Point out each leukocyte.
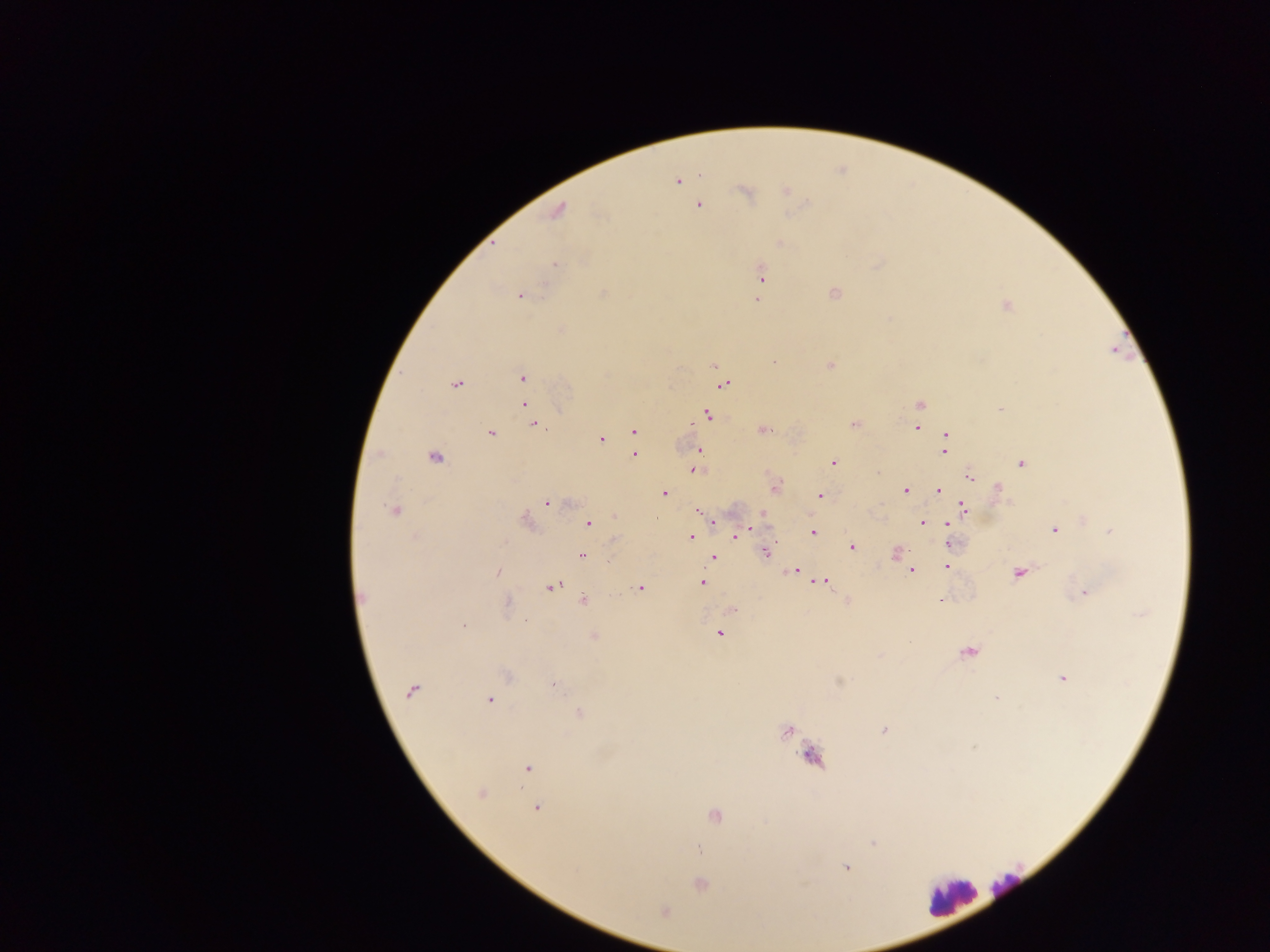
Approximate centers as [x, y] in pixels.
Leukocytes: [1007, 886], [952, 896].

Summary:
  - Plasmodium parasite locations: [700, 175], [677, 180], [786, 190], [744, 192], [698, 206], [558, 211], [781, 243], [555, 263], [761, 274], [604, 293], [835, 293], [520, 295], [756, 300], [1006, 306], [774, 363], [829, 365], [713, 366], [522, 377], [457, 383], [725, 384], [524, 405], [919, 405], [1000, 410], [708, 415], [854, 424], [538, 427], [916, 428], [634, 430], [764, 430], [491, 433], [946, 434], [601, 438], [699, 450], [944, 450], [635, 454], [435, 457], [833, 463], [1022, 463], [694, 470], [970, 477], [776, 486], [998, 487], [906, 490], [939, 491], [665, 493], [820, 496], [547, 502], [965, 508], [394, 510], [699, 511], [615, 517], [656, 518], [1083, 520], [526, 521], [923, 522], [588, 524], [948, 524], [1054, 529], [746, 531], [1109, 531], [813, 532], [737, 535], [691, 538], [615, 541], [949, 544], [852, 548], [896, 552], [767, 553], [582, 555], [713, 557], [908, 566], [947, 566], [793, 570], [911, 571], [497, 572], [1018, 573], [823, 582], [702, 583], [552, 586], [639, 588], [1086, 592], [362, 597], [584, 601], [847, 601], [941, 601], [508, 604], [732, 609], [463, 625], [719, 633], [593, 636], [967, 652], [506, 676], [1063, 678], [554, 683], [411, 691], [995, 699], [490, 700], [579, 714], [884, 731], [788, 732], [975, 746], [813, 758], [527, 769], [480, 794], [537, 808], [715, 815], [873, 843], [698, 849], [846, 867], [700, 884], [664, 910]
  - Field of view: single
  - Country: Ghana
  - Capture: mobile-phone photograph through a microscope
  - Image size: 1270×952 pixels
  - Preparation: thick blood film